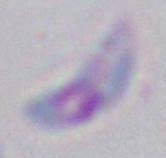

Summary:
  - Identification: Toxoplasma gondii
  - Magnification: 1000x
  - Modality: micrograph